Name the parasite shown.
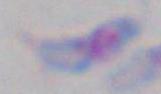

Toxoplasma gondii.

Summary:
  - Modality: photomicrograph
  - Magnification: 1000x